Name the cell type shown.
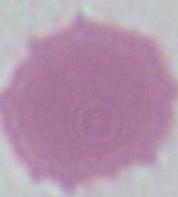

This is an erythrocyte.

Summary:
  - Magnification: 1000x
  - Modality: photomicrograph